Classify this cell by malaria status.
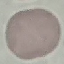
It is uninfected.

Summary:
  - Capture: smartphone through the microscope eyepiece
  - Stain: Giemsa
  - Preparation: thin blood film
  - Image type: cell patch, automatically extracted from a larger field of view and resized to 64 × 64 pixels